Classify this cell by malaria status.
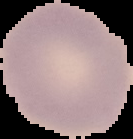

It is uninfected.

Segmented cell region on a black background. Image is 133×139 pixels. From a thin blood smear.